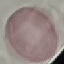

Summary:
  - Result: no malaria parasites detected
  - Stain: Giemsa
  - Capture: smartphone camera at the microscope eyepiece
  - Image type: automatically extracted cell patch, resized to 64 × 64 pixels
  - Preparation: thin blood smear